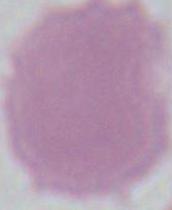
magnification: 1000x
modality: photomicrograph
identification: erythrocyte